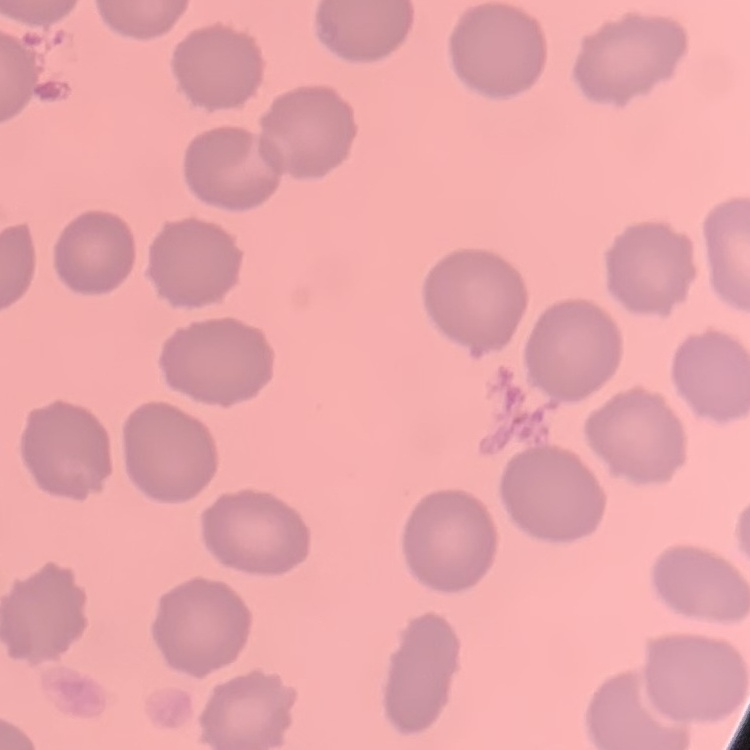
The red blood cells exhibit no rouleaux formation. Square crop of a larger photomicrograph. Thin blood smear. Field's or Giemsa stain.